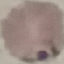

Result: malaria parasites identified. Photographed with a smartphone camera at the microscope eyepiece. Giemsa stain. Cell patch, automatically extracted from a larger field of view and resized to 64 × 64 pixels. Thin blood smear.